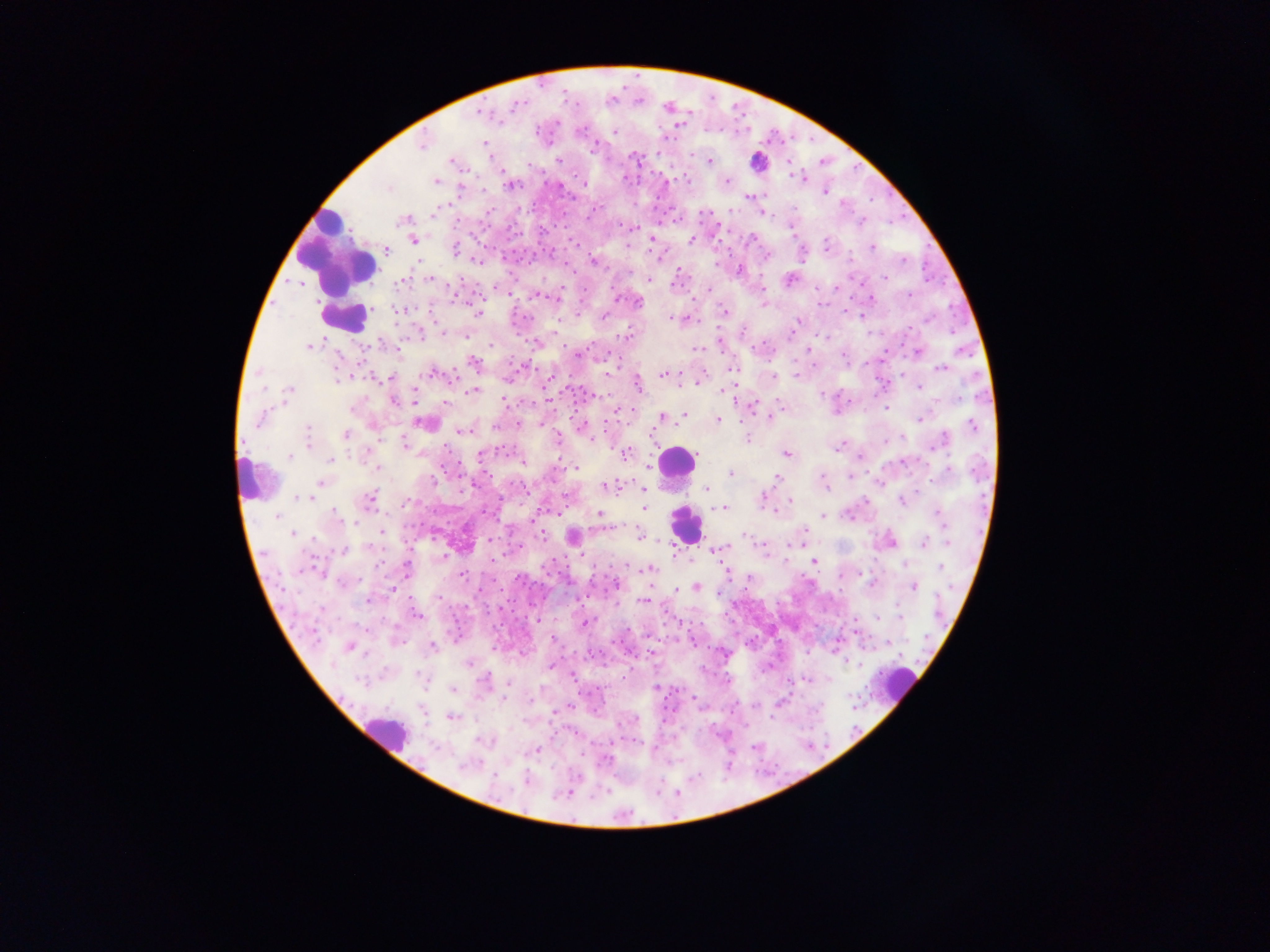 Approximate centers as x y in pixels. Plasmodium parasite locations: 520 102; 514 107; 666 110; 483 112; 557 122; 499 123; 614 131; 670 137; 667 139; 420 144; 594 145; 591 148; 634 158; 560 161; 709 162; 449 163; 790 172; 794 175; 623 178; 683 179; 802 179; 727 181; 583 184; 509 186; 560 187; 388 190; 826 192; 751 195; 748 197; 591 212; 765 214; 862 222; 628 226; 635 226; 790 230; 751 239; 414 241; 692 241; 872 247; 457 249; 903 259; 474 260; 593 260; 718 262; 739 268; 674 272; 677 276; 882 276; 647 280; 836 289; 539 296; 616 296; 910 296; 455 299; 870 299; 761 305; 823 306; 722 310; 476 313; 606 314; 929 318; 674 319; 799 322; 796 324; 441 330; 742 331; 420 332; 322 340; 719 342; 490 343; 307 345; 575 352; 917 353; 337 355; 473 362; 942 368; 431 373; 511 373; 661 375; 773 375; 798 376; 356 377; 390 380; 918 387; 290 391; 724 391; 472 392; 415 401; 396 402; 506 402; 445 403; 779 406; 751 408; 619 409; 885 409; 774 414; 684 415; 661 417; 770 417; 257 420; 718 420; 921 420; 541 423; 494 424; 972 425; 307 429; 461 431; 345 434; 653 436; 306 437; 558 438; 747 438; 946 438; 405 443; 308 444; 936 444; 838 448; 241 451; 785 454; 480 455; 625 455; 697 455; 288 456; 861 459; 330 461; 524 464; 648 465; 573 468; 376 469; 730 473; 850 476; 821 477; 775 479; 320 482; 605 485; 825 485; 469 487; 610 488; 647 488; 706 489; 297 497; 369 497; 764 498; 902 500; 789 501; 405 502; 722 508; 645 509; 770 512; 940 512; 337 513; 599 513; 822 515; 278 518; 355 521; 801 527; 381 530; 541 534; 640 535; 292 536; 744 537; 314 538; 925 541; 948 542; 789 543; 796 543; 762 549; 341 550; 442 556; 498 558; 784 561; 813 562; 627 565; 906 565; 903 566; 379 567; 409 567; 941 568; 651 569; 315 572; 463 575; 748 578; 612 585; 696 586; 915 586; 394 589; 676 591; 367 598; 440 599; 643 599; 321 610; 899 613; 417 614; 879 618; 536 619; 584 623; 693 641; 889 642; 349 645; 432 646; 651 654; 722 654; 367 657; 469 663; 553 663; 850 663; 550 665; 574 674; 484 679; 811 679; 805 681; 510 682; 655 687; 501 700; 753 703; 570 707; 754 707; 553 711; 770 716; 753 746; 606 760; 461 767; 493 778; 524 781. Thick blood smear. Collected in Ghana. Mobile-phone photograph taken through the microscope. One field of view. Image is 1270×952 pixels.